Report the malaria status of this cell.
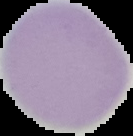

Uninfected.

Summary:
  - Image type: cell region segmented out of the field of view; surrounding area masked to black
  - Image size: 133×136 pixels
  - Preparation: thin blood smear